Outline each blood parasite and name the species.
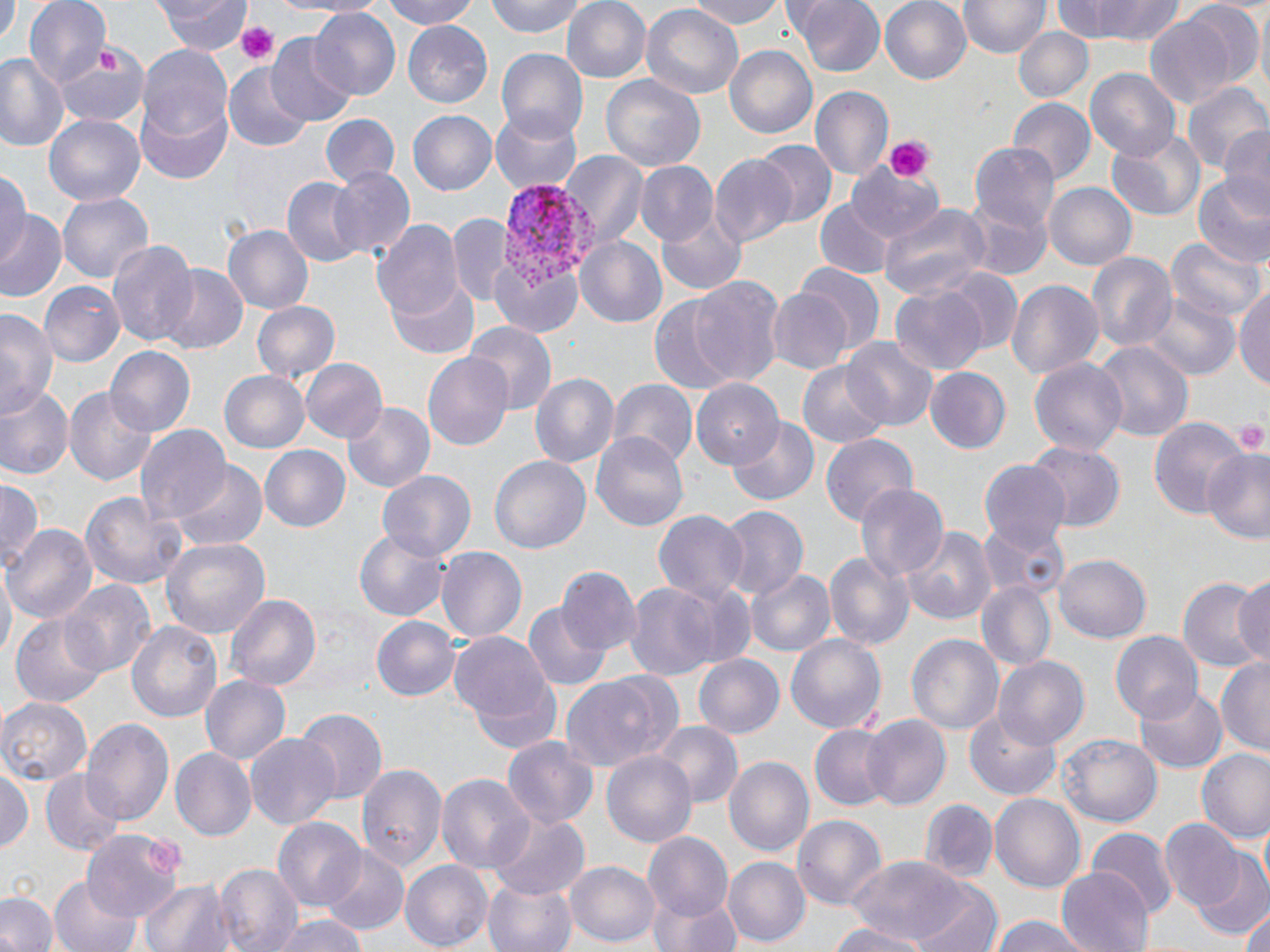

Approximate bounding boxes as (x1,y1)-(x2,y2) corner pairs in pixels.
Plasmodium vivax-infected red blood cells: (499,181)-(600,296).
No Plasmodium falciparum, Plasmodium ovale, Plasmodium malariae, Babesia divergens, or Trypanosoma brucei observed.

slide_level_diagnosis: Plasmodium vivax
magnification: 1000x
image_size: 1270×952 pixels
preparation: thin blood film
stain: May-Grünwald-Giemsa
modality: optical microscopy
platelet_locations: 'approximate bounding boxes as (x1,y1)-(x2,y2) corner pairs in pixels: (237,21)-(280,64), (880,135)-(932,182), (1232,419)-(1268,457)'
uninfected_red_blood_cell_locations: 'approximate bounding boxes as (x1,y1)-(x2,y2) corner pairs in pixels: (23,0)-(110,87), (156,0)-(250,53), (295,0)-(384,17), (375,0)-(483,29), (485,0)-(594,39), (560,0)-(654,85), (692,0)-(790,28), (790,0)-(883,77), (879,0)-(974,85), (961,0)-(1048,60), (1048,0)-(1189,46), (1,4)-(19,41), (639,4)-(744,100), (309,9)-(400,101), (1144,11)-(1243,111), (402,22)-(494,107), (1013,24)-(1094,103), (264,34)-(358,126), (724,43)-(817,141), (55,44)-(148,128), (137,44)-(233,140), (495,46)-(590,138), (0,55)-(69,153), (223,66)-(311,151), (1086,70)-(1181,160), (600,76)-(704,171), (1184,78)-(1268,175), (810,87)-(892,184), (138,96)-(232,185), (1008,98)-(1095,186), (489,107)-(583,194), (406,110)-(497,196), (43,111)-(147,209), (320,115)-(399,191), (1219,124)-(1270,214), (1106,130)-(1203,220), (757,140)-(836,228), (971,143)-(1059,231), (562,152)-(648,249), (710,154)-(798,249), (850,160)-(939,245), (634,162)-(718,246), (0,166)-(29,268), (327,167)-(415,260), (1192,174)-(1270,267), (281,175)-(369,268), (1045,183)-(1135,269), (57,190)-(153,283), (963,194)-(1051,283), (815,200)-(893,278), (655,201)-(747,295), (880,201)-(992,303), (1,211)-(67,300), (372,217)-(464,323), (449,217)-(515,308), (223,226)-(312,312), (1168,235)-(1265,324), (575,236)-(667,330), (107,240)-(198,351), (1087,251)-(1176,355), (795,264)-(885,356), (155,265)-(249,356), (942,267)-(1023,355), (689,274)-(787,390), (390,277)-(481,360), (1005,280)-(1104,384), (41,282)-(126,370), (1234,284)-(1270,392), (892,285)-(990,375), (768,289)-(853,373), (1146,295)-(1238,380), (647,297)-(737,398), (251,300)-(338,385), (0,307)-(61,423), (468,321)-(555,412), (840,337)-(939,434), (1095,341)-(1193,444), (106,347)-(195,438), (422,350)-(514,451), (300,357)-(386,444), (1029,357)-(1129,458), (797,360)-(893,449), (925,369)-(1011,454), (220,370)-(309,452), (530,372)-(619,471), (691,379)-(781,468), (611,381)-(697,469), (0,384)-(76,482), (66,387)-(159,487), (341,401)-(434,493), (1148,414)-(1248,518), (728,420)-(818,505), (136,426)-(230,525), (591,431)-(691,530), (821,433)-(918,528), (1025,442)-(1126,534), (261,447)-(351,531), (1203,449)-(1270,543), (488,454)-(591,556), (979,459)-(1071,556), (165,460)-(270,556), (378,470)-(476,564), (0,479)-(42,573), (854,484)-(948,581), (79,489)-(190,588), (716,506)-(808,598), (652,511)-(747,605), (978,520)-(1072,602), (10,525)-(95,622), (902,525)-(999,624), (355,530)-(452,621), (160,534)-(269,637), (437,548)-(526,645), (825,551)-(915,653), (1054,554)-(1150,643), (1,564)-(16,667), (556,568)-(640,659), (746,569)-(837,658), (1180,574)-(1268,676), (1231,575)-(1270,665), (59,579)-(158,680), (622,581)-(725,680), (976,581)-(1057,673), (226,594)-(321,693), (523,600)-(612,692), (11,613)-(108,710), (371,616)-(460,702), (127,620)-(224,724), (450,628)-(557,737), (1111,633)-(1202,724), (785,634)-(887,733), (907,634)-(1005,736), (692,653)-(784,740), (1217,655)-(1270,758), (993,656)-(1090,752), (559,673)-(675,770), (200,675)-(291,768), (1133,684)-(1226,773), (0,697)-(91,787), (294,708)-(384,806), (965,709)-(1064,801), (861,715)-(951,811), (81,716)-(173,825), (649,720)-(743,811), (810,726)-(893,811), (245,734)-(342,830), (1058,734)-(1162,828), (502,737)-(596,833), (171,747)-(255,840), (1195,748)-(1270,842), (602,751)-(698,849), (724,754)-(815,861), (358,763)-(446,875), (1,764)-(34,855), (41,772)-(126,856), (437,772)-(533,876), (990,791)-(1084,892), (918,800)-(997,884), (484,809)-(591,902), (793,814)-(888,911), (273,817)-(368,912), (1160,820)-(1244,914), (1089,827)-(1177,919), (84,829)-(182,921), (643,833)-(735,925), (320,849)-(410,935), (723,856)-(810,946), (1192,856)-(1270,942), (848,857)-(972,951), (399,859)-(492,951), (566,859)-(660,947), (215,864)-(301,952), (1057,866)-(1153,951), (483,873)-(577,952), (47,877)-(144,952), (139,879)-(229,952), (911,880)-(1003,952), (299,884)-(407,952), (649,891)-(741,952), (0,892)-(56,952), (1238,912)-(1269,952), (270,915)-(370,952), (986,916)-(1097,952), (823,923)-(935,952)'
field_of_view: single